Identify the blood parasite species.
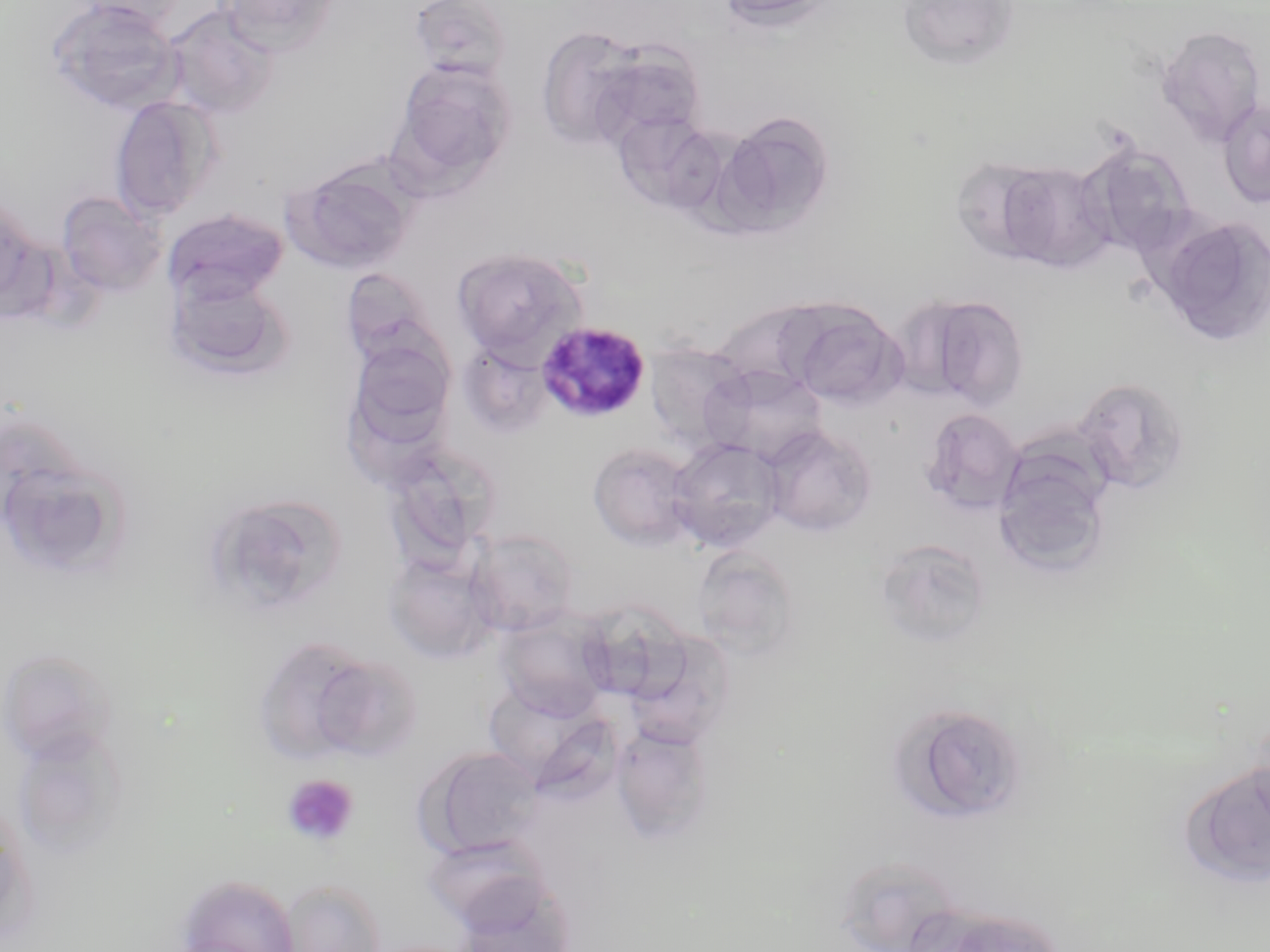

Plasmodium malariae.

modality = optical microscopy
Plasmodium malariae-infected red blood cell locations = approximate bounding boxes as (x1,y1)-(x2,y2) corner pairs in pixels: (536,321)-(651,423)
field of view = one of a larger specimen
image size = 1270×952 pixels
stain = May-Grünwald-Giemsa
platelet locations = approximate bounding boxes as (x1,y1)-(x2,y2) corner pairs in pixels: (283,774)-(359,847)
preparation = thin blood film
uninfected red blood cell locations = approximate bounding boxes as (x1,y1)-(x2,y2) corner pairs in pixels: (44,0)-(184,116), (76,0)-(189,29), (217,0)-(340,54), (408,0)-(515,83), (713,0)-(842,32), (900,0)-(1021,72), (163,4)-(281,121), (535,25)-(650,149), (1155,25)-(1266,145), (586,40)-(708,151), (390,59)-(518,186), (110,94)-(222,221), (1217,98)-(1270,208), (713,111)-(836,237), (612,112)-(724,214), (1076,142)-(1196,258), (948,155)-(1060,264), (991,160)-(1114,272), (286,163)-(415,274), (56,191)-(167,296), (164,208)-(289,304), (1154,215)-(1270,347), (452,247)-(586,360), (341,267)-(443,369), (166,273)-(292,381), (908,293)-(1031,410), (715,299)-(835,411), (783,300)-(905,409), (345,337)-(456,451), (459,341)-(553,439), (643,343)-(751,452), (704,364)-(827,466), (1072,376)-(1190,496), (920,407)-(1024,516), (762,425)-(877,537), (667,437)-(787,553), (992,440)-(1114,577), (380,441)-(502,570), (587,441)-(701,551), (11,468)-(140,574), (203,493)-(351,608), (466,528)-(579,636), (875,537)-(992,650), (692,546)-(804,660), (383,553)-(498,664), (574,604)-(689,706), (496,613)-(610,720), (622,631)-(735,750), (252,636)-(383,766), (0,646)-(118,766), (306,651)-(425,762), (494,694)-(623,796), (888,701)-(1030,825), (610,724)-(716,844), (10,728)-(130,861), (417,746)-(546,859), (1180,758)-(1270,890), (0,801)-(34,942), (420,833)-(553,930), (834,854)-(966,952), (176,874)-(300,952), (448,876)-(578,950), (277,878)-(388,952), (933,908)-(1065,952)
magnification = 1000x